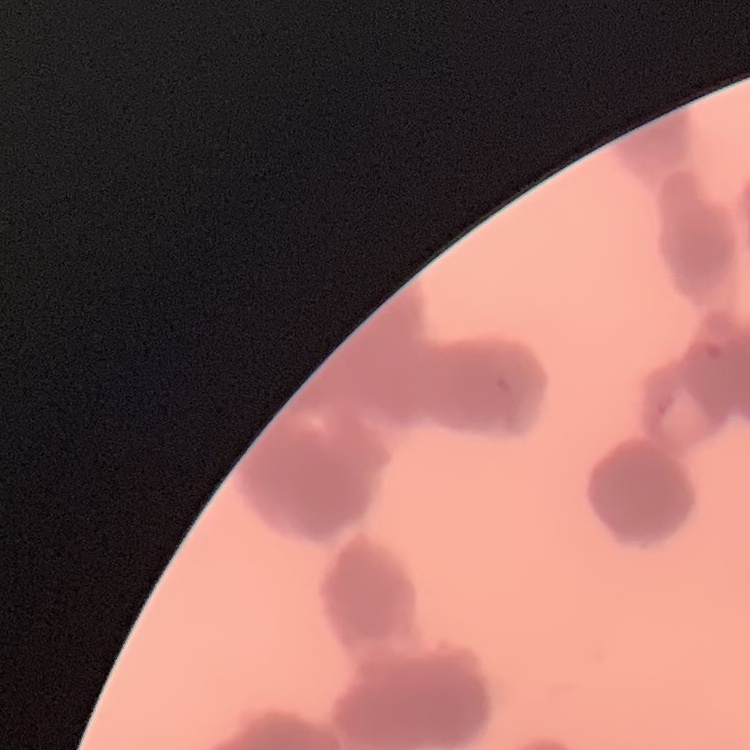

Summary:
  - Erythrocyte morphology: rouleaux formation
  - Stain: Field's or Giemsa
  - Image type: one tile cut from a larger photomicrograph
  - Preparation: thin blood smear